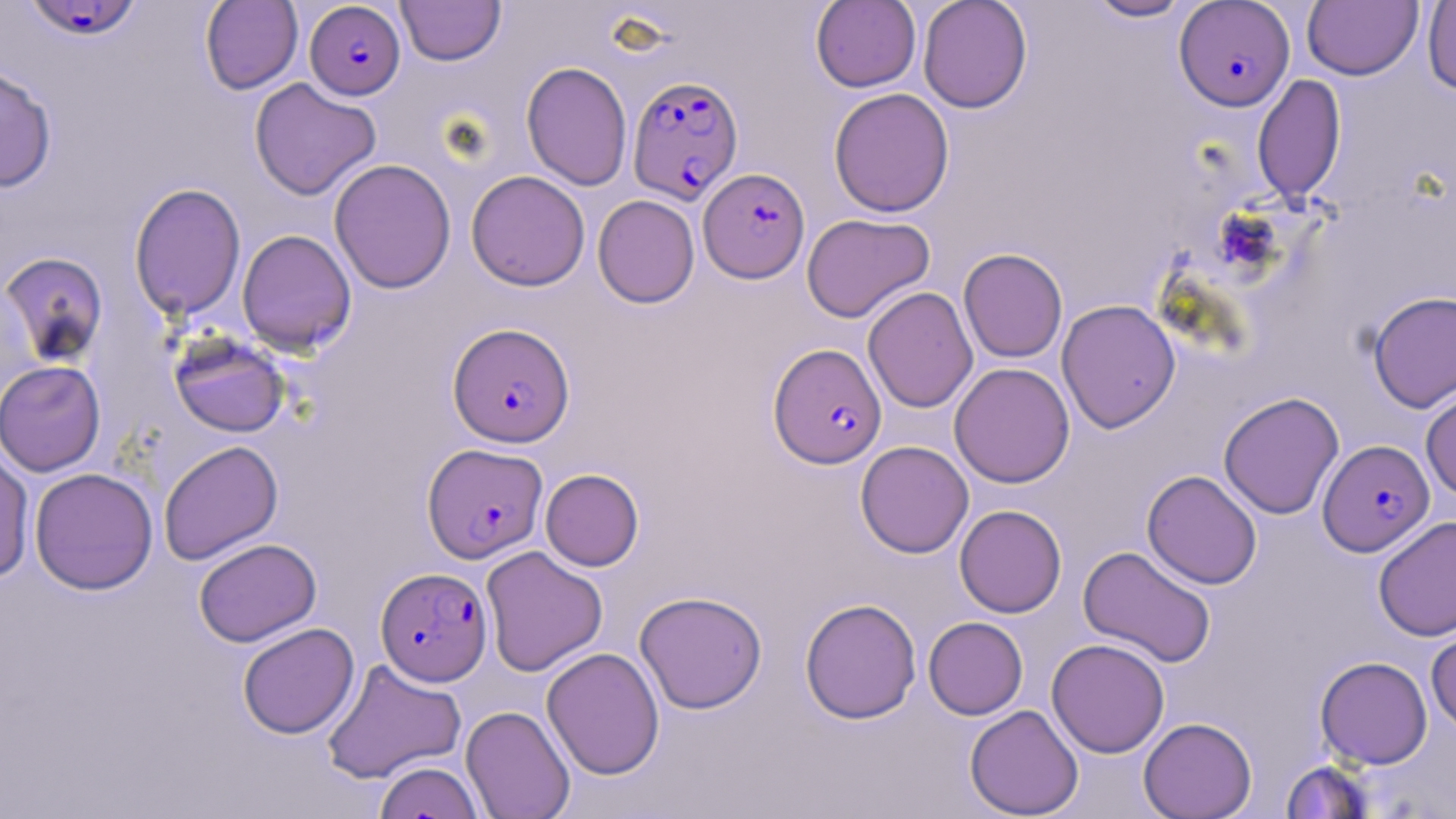
Summary:
  - Coordinate format: approximate bounding boxes as (x1, y1, x2, y2) in pixels
  - Plasmodium falciparum-infected red blood cell locations: (24, 0, 143, 42), (305, 1, 406, 100), (1174, 1, 1295, 111), (627, 75, 743, 204), (699, 168, 810, 283), (448, 322, 575, 448), (769, 343, 886, 468), (1318, 440, 1435, 556), (422, 443, 548, 563), (375, 567, 492, 686)
  - Uninfected red blood cell locations: (200, 0, 302, 94), (396, 0, 505, 65), (918, 0, 1032, 113), (1083, 0, 1195, 22), (810, 1, 921, 92), (1302, 1, 1423, 80), (1422, 1, 1456, 95), (521, 61, 632, 191), (0, 62, 58, 193), (1252, 74, 1346, 205), (249, 78, 381, 200), (828, 88, 955, 217), (329, 158, 457, 294), (466, 170, 591, 291), (129, 182, 246, 321), (593, 194, 700, 308), (801, 213, 936, 323), (237, 229, 357, 355), (958, 248, 1068, 363), (1, 251, 109, 368), (862, 286, 978, 413), (1368, 290, 1456, 412), (1056, 299, 1180, 433), (169, 333, 291, 438), (1, 360, 105, 477), (949, 362, 1075, 488), (1420, 384, 1456, 502), (1218, 391, 1345, 519), (158, 440, 283, 566), (855, 441, 974, 558), (0, 445, 35, 584), (29, 467, 158, 595), (540, 468, 644, 571), (1142, 470, 1263, 589), (954, 504, 1067, 618), (1373, 515, 1456, 642), (193, 538, 321, 647), (1078, 545, 1216, 668), (480, 546, 608, 677), (634, 590, 767, 714), (799, 598, 922, 724), (923, 616, 1028, 720), (237, 622, 359, 739), (1426, 622, 1456, 735), (1046, 638, 1169, 758), (541, 647, 665, 780), (1315, 656, 1432, 769), (321, 658, 467, 784), (460, 704, 575, 819), (964, 704, 1084, 818), (1138, 717, 1256, 818), (373, 760, 485, 819), (1281, 760, 1376, 818)
  - Slide-level diagnosis: Plasmodium falciparum
  - Magnification: 1000x
  - Stain: May-Grünwald-Giemsa
  - Field of view: single
  - Modality: optical microscopy
  - Image size: 1456×819 pixels
  - Preparation: thin blood smear